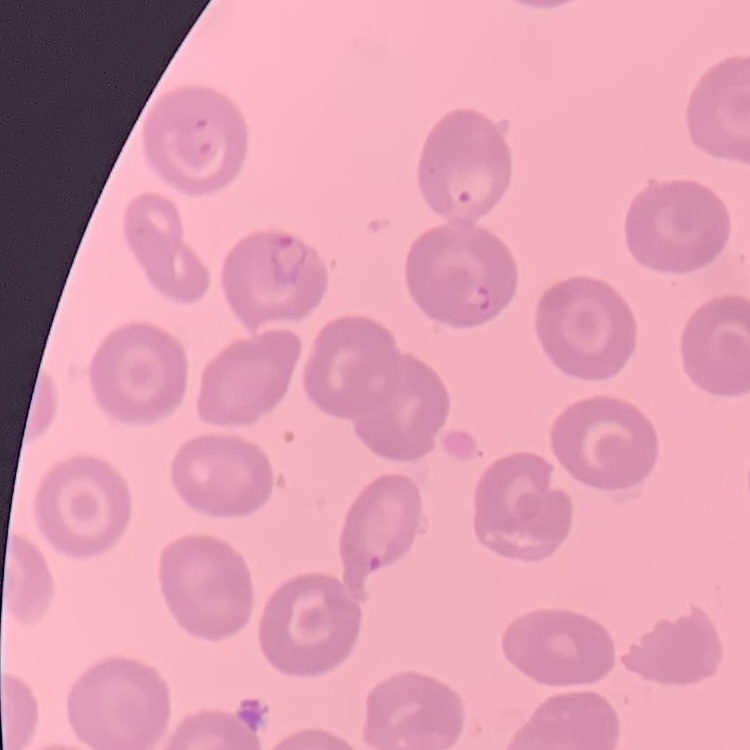 The red blood cells show no rouleaux formation. One tile cut from a larger photomicrograph. Field's or Giemsa stain. Thin blood film.